Identify the blood parasite species.
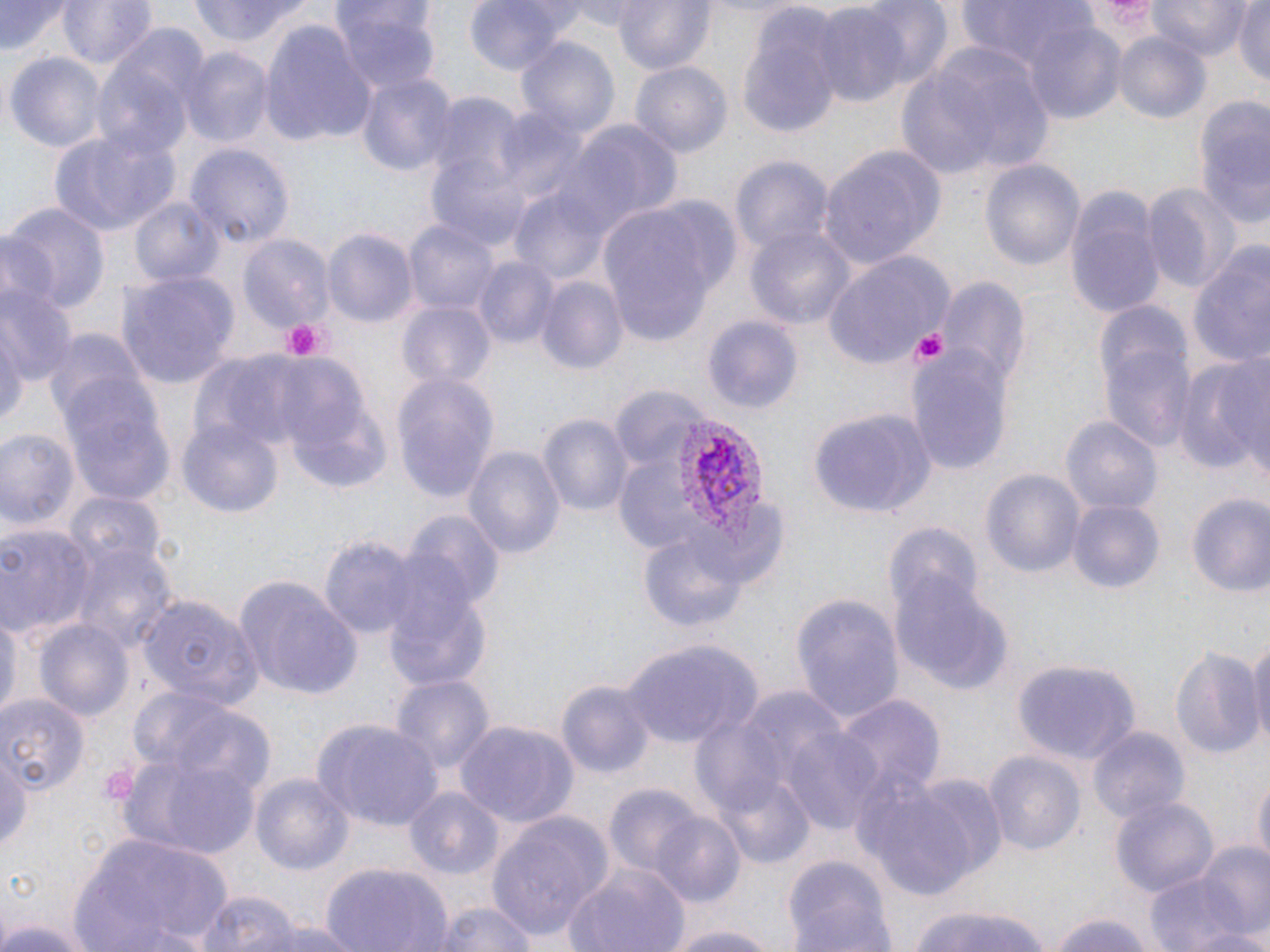

Plasmodium vivax.

Summary:
  - Coordinate format: approximate bounding boxes as (x1, y1, x2, y2) in pixels
  - Platelet locations: (282, 318, 328, 360), (909, 327, 952, 370), (98, 763, 140, 808)
  - Plasmodium vivax-infected red blood cell locations: (674, 414, 768, 549)
  - Uninfected red blood cell locations: (0, 0, 68, 59), (62, 0, 155, 71), (189, 0, 313, 45), (465, 0, 580, 73), (566, 0, 656, 33), (610, 0, 716, 76), (852, 0, 953, 89), (953, 0, 1106, 77), (1077, 0, 1168, 53), (1146, 0, 1252, 60), (1232, 1, 1270, 88), (809, 4, 914, 110), (334, 5, 439, 98), (736, 7, 846, 137), (1017, 16, 1129, 125), (260, 20, 375, 146), (1114, 35, 1211, 122), (516, 36, 621, 142), (897, 39, 1056, 182), (93, 41, 201, 163), (182, 46, 274, 146), (7, 50, 108, 152), (630, 63, 731, 160), (355, 71, 459, 180), (424, 91, 523, 194), (1188, 97, 1270, 235), (539, 115, 680, 246), (48, 126, 181, 235), (185, 143, 294, 248), (818, 143, 944, 267), (428, 152, 536, 252), (731, 159, 833, 258), (981, 160, 1084, 273), (1142, 181, 1241, 293), (1065, 185, 1162, 320), (514, 194, 610, 282), (132, 196, 226, 289), (597, 199, 730, 349), (4, 205, 110, 317), (405, 219, 500, 317), (745, 226, 854, 333), (324, 227, 417, 325), (0, 231, 58, 316), (238, 235, 334, 334), (1188, 243, 1270, 373), (822, 250, 952, 369), (473, 255, 559, 348), (118, 269, 240, 388), (535, 275, 627, 377), (935, 275, 1032, 394), (1, 280, 75, 388), (398, 301, 496, 388), (0, 313, 25, 439), (704, 314, 802, 413), (1095, 318, 1198, 454), (907, 342, 1013, 472), (1174, 349, 1266, 477), (227, 353, 317, 445), (281, 358, 371, 446), (391, 373, 499, 503), (62, 383, 175, 503), (612, 390, 696, 457), (291, 400, 393, 494), (811, 411, 936, 517), (538, 412, 632, 519), (1061, 415, 1165, 516), (180, 420, 281, 520), (0, 430, 80, 534), (463, 445, 565, 563), (618, 460, 697, 549), (982, 470, 1083, 576), (66, 492, 167, 578), (1185, 493, 1270, 602), (1068, 498, 1164, 597), (692, 505, 786, 586), (403, 512, 503, 614), (885, 521, 987, 632), (2, 524, 98, 638), (640, 527, 753, 639), (319, 536, 421, 639), (67, 538, 179, 655), (892, 568, 1013, 696), (231, 575, 364, 699), (385, 590, 493, 693), (792, 592, 902, 722), (139, 595, 260, 711), (1, 603, 18, 725), (36, 618, 135, 724), (1247, 632, 1270, 753), (621, 638, 762, 749), (1171, 645, 1266, 764), (1012, 659, 1142, 762), (389, 675, 494, 777), (558, 678, 656, 780), (131, 689, 274, 797), (832, 693, 945, 801), (0, 694, 88, 797), (456, 719, 577, 832), (314, 720, 441, 834), (1088, 726, 1188, 826), (785, 728, 884, 835), (984, 750, 1086, 860), (117, 753, 262, 858), (0, 756, 30, 858), (850, 766, 993, 903), (1253, 770, 1269, 873), (250, 775, 355, 873), (720, 775, 815, 870), (605, 783, 703, 878), (405, 788, 503, 881), (1111, 795, 1217, 898), (486, 808, 612, 940), (646, 811, 747, 907), (70, 828, 237, 952), (1189, 841, 1270, 940), (782, 854, 898, 952), (1144, 859, 1261, 952), (319, 860, 454, 952), (563, 863, 691, 952), (192, 889, 305, 952), (428, 901, 539, 952), (907, 904, 1058, 952), (1048, 911, 1159, 952), (258, 917, 361, 952), (0, 918, 102, 952), (659, 921, 784, 952), (1184, 926, 1270, 952)
  - Stain: May-Grünwald-Giemsa
  - Field of view: single
  - Modality: light microscopy
  - Preparation: thin blood smear
  - Magnification: 1000x
  - Image size: 1270×952 pixels